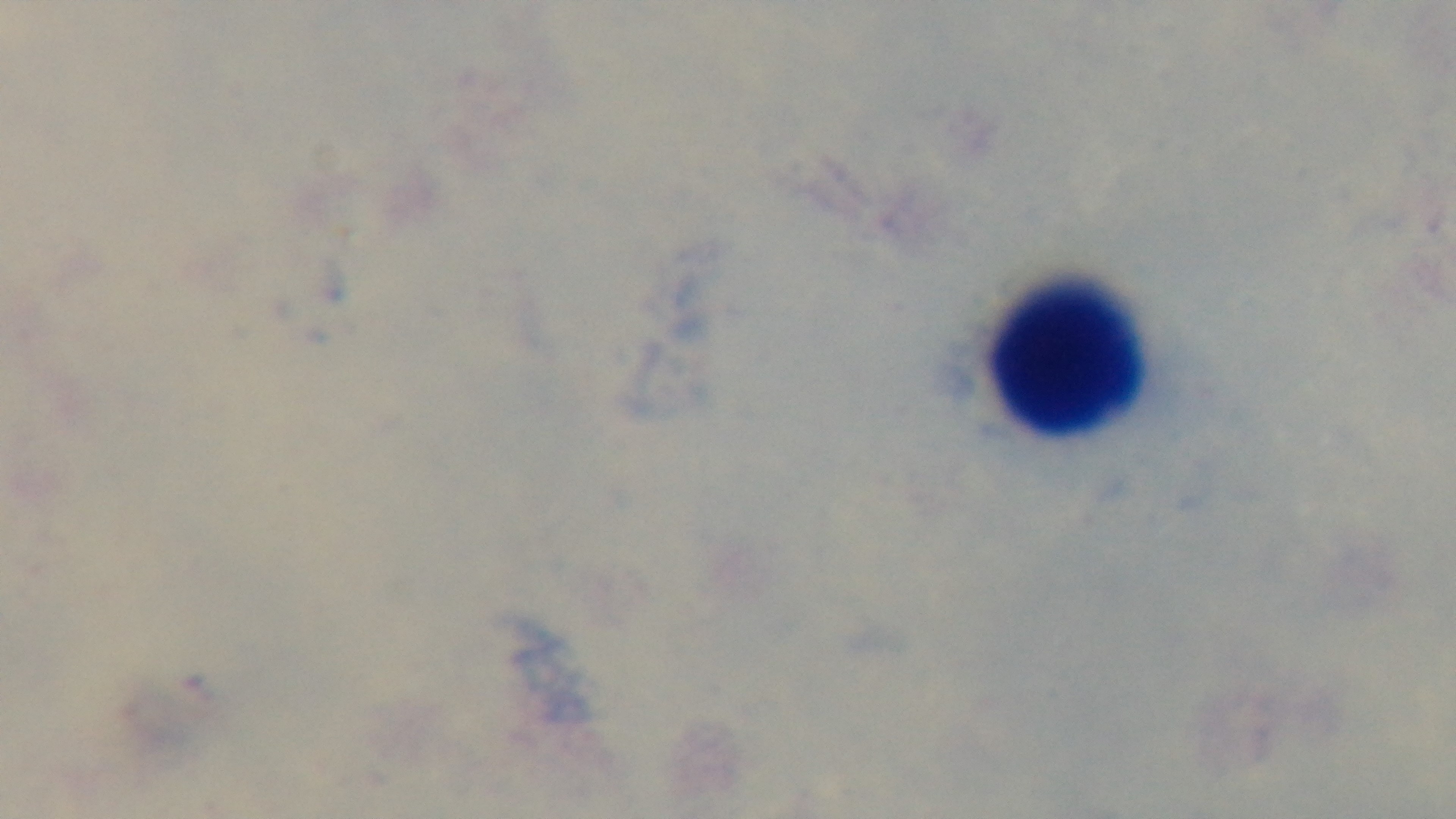
Summary:
  - Modality: light microscopy
  - Field of view: one from the slide
  - Stain: Giemsa
  - Malaria status: uninfected
  - Objective: 100x oil immersion
  - Capture: mounted 4K digital camera
  - Preparation: thick